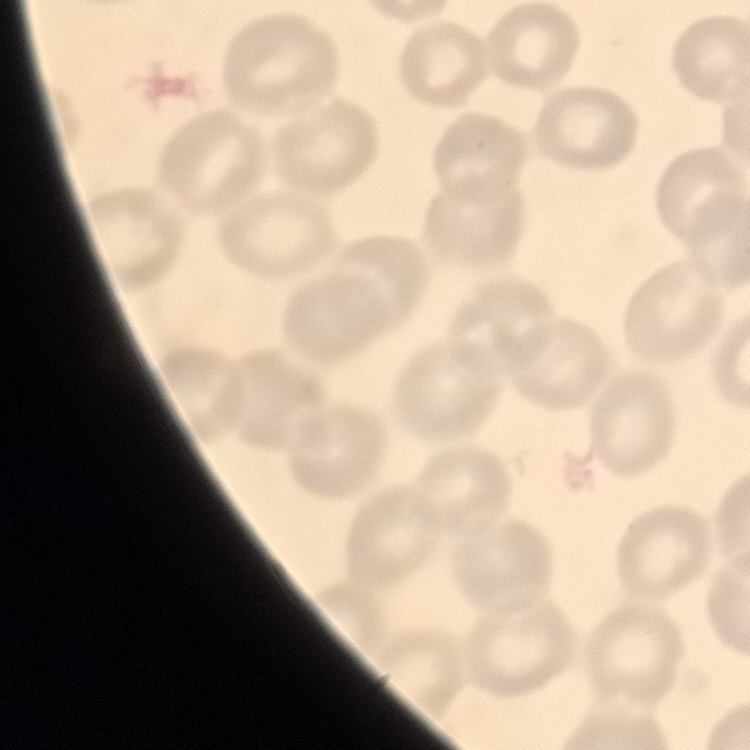

The red blood cells show no rouleaux formation. Stained with either Field's or Giemsa. Thin blood smear. Square crop of a larger photomicrograph.